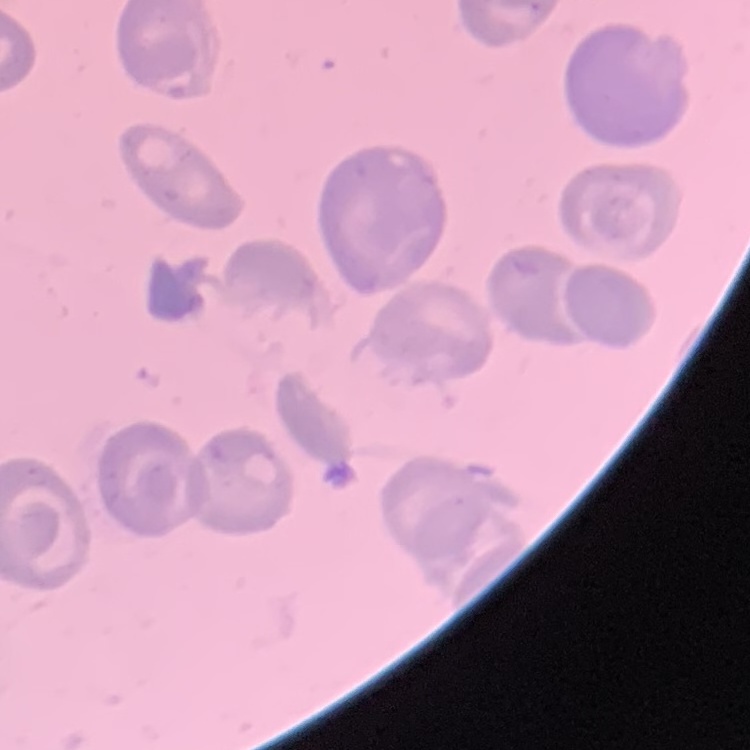
red_blood_cell_morphology: no rouleaux formation
image_type: square crop of a larger photomicrograph
preparation: thin blood film
stain: Field's or Giemsa